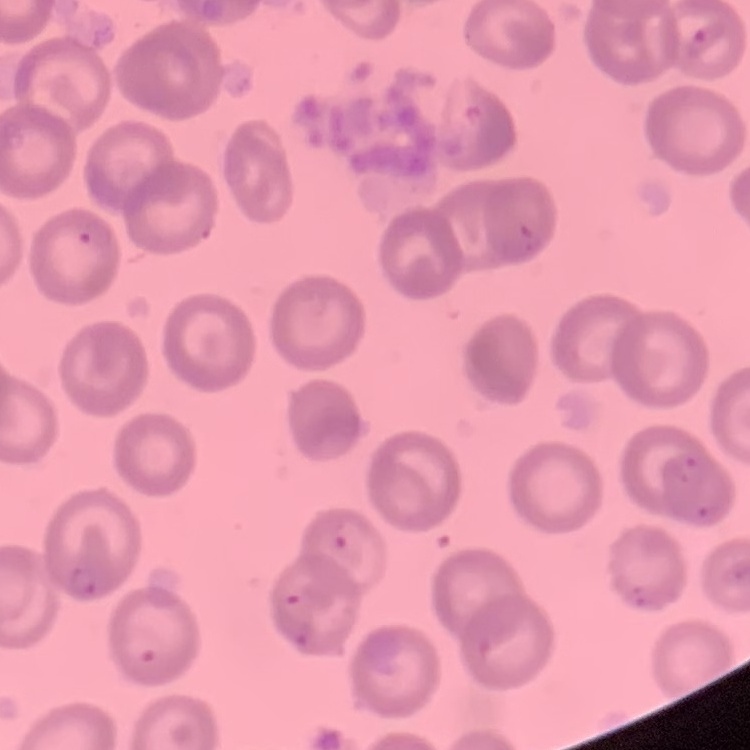 The red blood cells exhibit no rouleaux formation. Thin blood film. One tile cut from a larger photomicrograph. Stained with either Field's or Giemsa.